Point out each Plasmodium parasite.
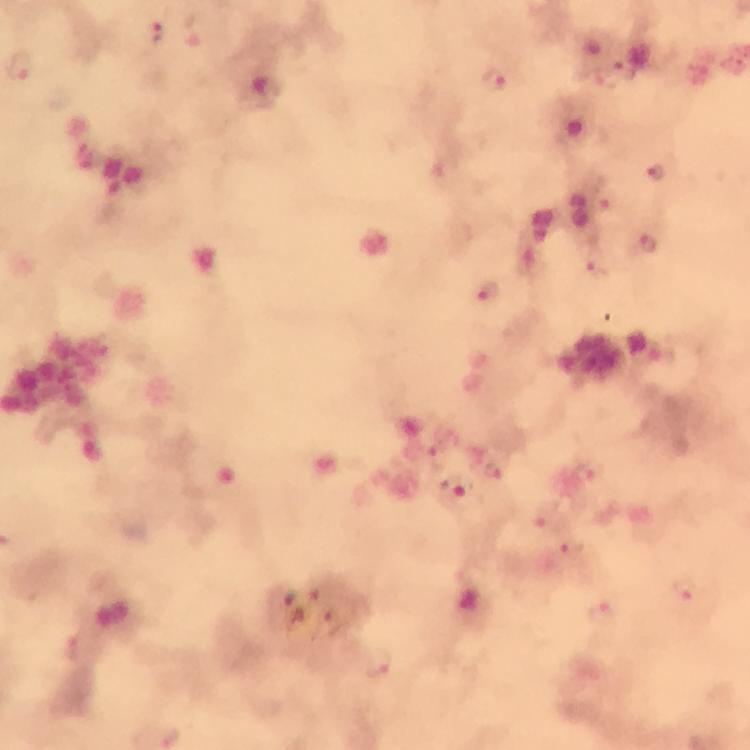

Approximate centers as [x, y] in pixels.
Plasmodium parasites: [157, 30], [21, 65], [496, 80], [267, 89], [657, 173], [448, 175], [648, 245], [594, 267], [489, 294], [435, 445], [495, 470], [590, 471], [456, 494], [545, 514], [573, 545], [685, 589], [602, 615], [380, 663].

immersion_oil: used
preparation: thick blood film
image_size: 750×750 pixels
stain: Giemsa
capture: smartphone camera through the microscope
context: from a malaria diagnostic workup
magnification: 100x
cropped_from: one field of view